Locate and identify every blood parasite.
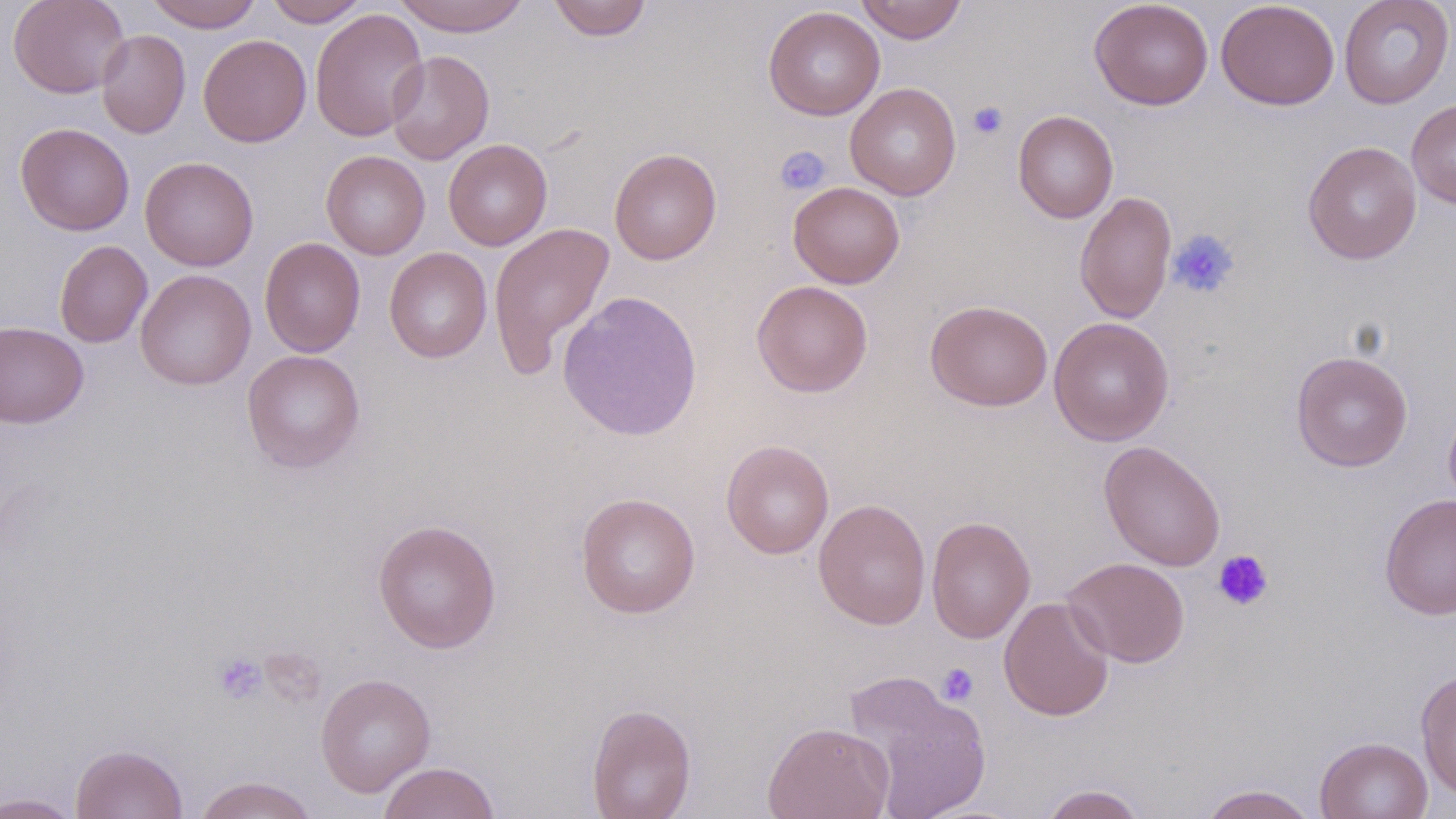

No blood parasites seen.

Summary:
  - Coordinate format: approximate bounding boxes as named x1/y1/x2/y2 corners in pixels
  - Platelet locations: (x1=968, y1=101, x2=1009, y2=139), (x1=773, y1=145, x2=831, y2=196), (x1=1167, y1=228, x2=1240, y2=299), (x1=1213, y1=549, x2=1273, y2=611), (x1=213, y1=652, x2=267, y2=705), (x1=936, y1=663, x2=980, y2=706)
  - Uninfected red blood cell locations: (x1=8, y1=0, x2=130, y2=99), (x1=145, y1=0, x2=263, y2=31), (x1=263, y1=0, x2=370, y2=27), (x1=390, y1=0, x2=532, y2=36), (x1=547, y1=0, x2=653, y2=41), (x1=856, y1=0, x2=966, y2=44), (x1=1089, y1=0, x2=1214, y2=110), (x1=1215, y1=0, x2=1340, y2=110), (x1=1339, y1=0, x2=1455, y2=109), (x1=762, y1=6, x2=885, y2=120), (x1=310, y1=7, x2=429, y2=142), (x1=95, y1=29, x2=191, y2=138), (x1=197, y1=34, x2=312, y2=147), (x1=386, y1=50, x2=494, y2=165), (x1=845, y1=83, x2=961, y2=200), (x1=1406, y1=98, x2=1456, y2=209), (x1=1013, y1=110, x2=1119, y2=224), (x1=15, y1=122, x2=134, y2=236), (x1=443, y1=139, x2=552, y2=251), (x1=1302, y1=141, x2=1422, y2=264), (x1=609, y1=148, x2=722, y2=265), (x1=321, y1=150, x2=430, y2=260), (x1=140, y1=156, x2=259, y2=271), (x1=788, y1=182, x2=905, y2=289), (x1=1075, y1=190, x2=1177, y2=324), (x1=488, y1=222, x2=616, y2=376), (x1=260, y1=237, x2=365, y2=357), (x1=54, y1=240, x2=152, y2=348), (x1=384, y1=247, x2=492, y2=363), (x1=135, y1=269, x2=256, y2=390), (x1=751, y1=279, x2=873, y2=397), (x1=557, y1=290, x2=704, y2=443), (x1=925, y1=299, x2=1053, y2=411), (x1=1049, y1=316, x2=1175, y2=446), (x1=0, y1=322, x2=89, y2=427), (x1=241, y1=349, x2=366, y2=473), (x1=1290, y1=351, x2=1413, y2=471), (x1=1443, y1=398, x2=1456, y2=513), (x1=720, y1=440, x2=834, y2=559), (x1=1098, y1=440, x2=1226, y2=571), (x1=575, y1=491, x2=701, y2=619), (x1=1379, y1=494, x2=1456, y2=620), (x1=813, y1=498, x2=931, y2=629), (x1=926, y1=515, x2=1036, y2=644), (x1=372, y1=519, x2=501, y2=654), (x1=1062, y1=557, x2=1190, y2=668), (x1=999, y1=596, x2=1115, y2=721), (x1=1416, y1=669, x2=1456, y2=801), (x1=843, y1=670, x2=993, y2=819), (x1=315, y1=673, x2=436, y2=797), (x1=586, y1=703, x2=696, y2=819), (x1=763, y1=721, x2=893, y2=819), (x1=1314, y1=736, x2=1433, y2=819), (x1=70, y1=743, x2=189, y2=819), (x1=377, y1=762, x2=501, y2=819), (x1=193, y1=775, x2=320, y2=819), (x1=1038, y1=784, x2=1148, y2=819), (x1=1198, y1=784, x2=1319, y2=819), (x1=0, y1=792, x2=84, y2=819)
  - Slide-level diagnosis: negative for blood parasites
  - Field of view: single
  - Image size: 1456×819 pixels
  - Stain: May-Grünwald-Giemsa
  - Modality: optical microscopy
  - Magnification: 1000x
  - Preparation: thin blood film